Identify the parasite.
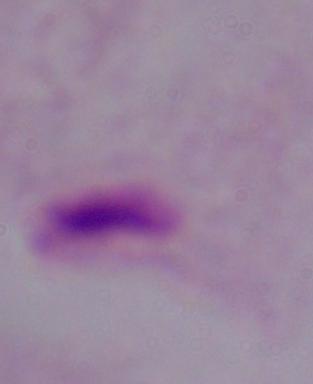
A trichomonad.

Summary:
  - Modality: micrograph
  - Magnification: 1000x